Locate every blood parasite and identify its species.
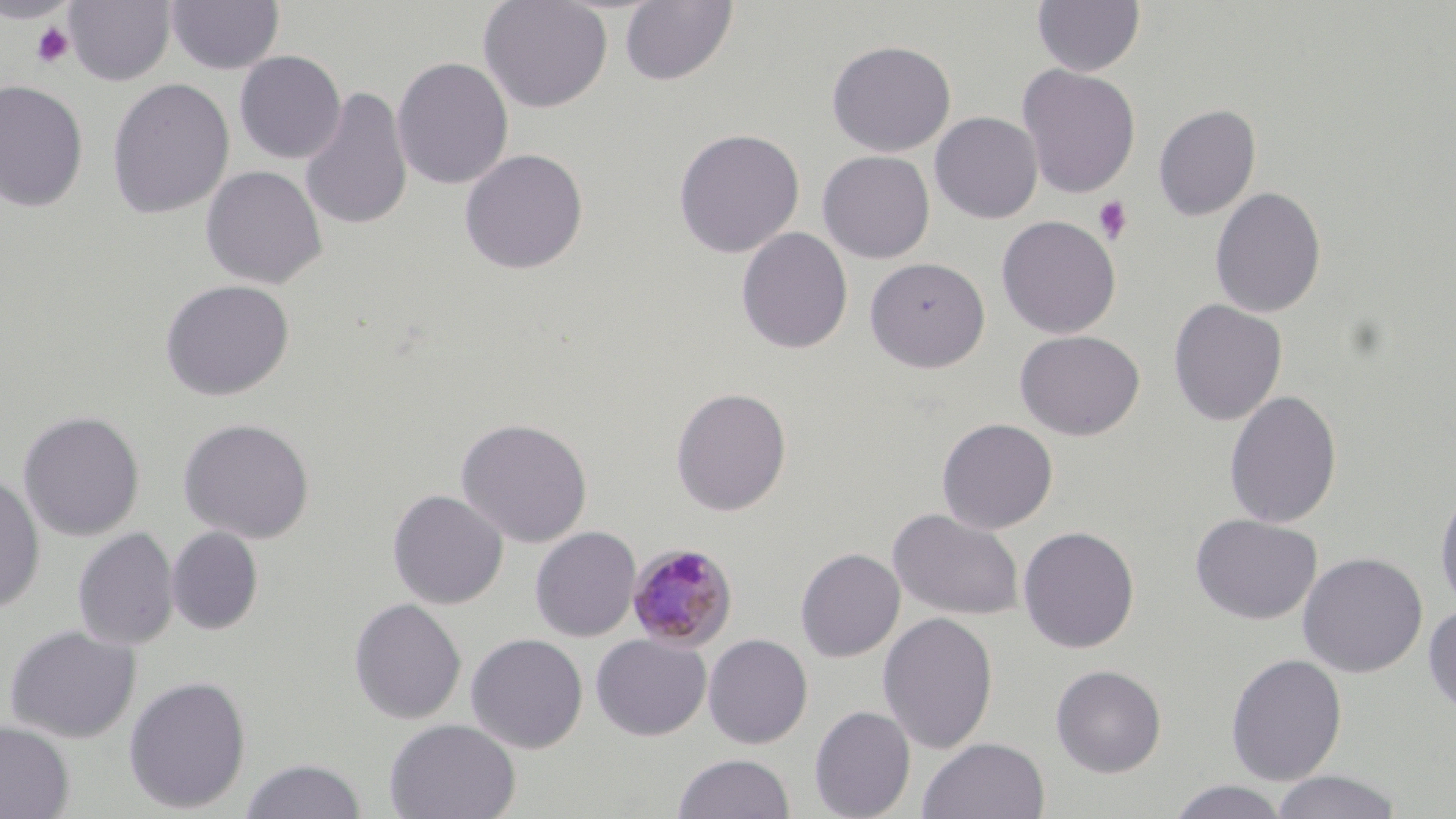
Approximate bounding boxes as named x1/y1/x2/y2 corners in pixels.
Plasmodium malariae-infected red blood cells: (x1=626, y1=542, x2=738, y2=652).
No Plasmodium falciparum, Plasmodium ovale, Plasmodium vivax, Babesia divergens, or Trypanosoma brucei observed.

Platelet locations: (x1=31, y1=21, x2=75, y2=68), (x1=1093, y1=196, x2=1132, y2=243). Uninfected red blood cell locations: (x1=0, y1=0, x2=80, y2=24), (x1=64, y1=0, x2=176, y2=86), (x1=166, y1=0, x2=284, y2=75), (x1=478, y1=0, x2=612, y2=114), (x1=1032, y1=0, x2=1146, y2=77), (x1=619, y1=1, x2=738, y2=86), (x1=18, y1=15, x2=82, y2=64), (x1=826, y1=39, x2=956, y2=157), (x1=234, y1=51, x2=346, y2=164), (x1=392, y1=57, x2=514, y2=190), (x1=1017, y1=64, x2=1141, y2=198), (x1=106, y1=78, x2=235, y2=220), (x1=0, y1=79, x2=89, y2=212), (x1=299, y1=85, x2=412, y2=231), (x1=1152, y1=103, x2=1261, y2=220), (x1=929, y1=112, x2=1043, y2=224), (x1=673, y1=128, x2=805, y2=258), (x1=459, y1=148, x2=588, y2=274), (x1=817, y1=150, x2=935, y2=263), (x1=201, y1=165, x2=326, y2=289), (x1=1210, y1=187, x2=1327, y2=318), (x1=996, y1=215, x2=1121, y2=338), (x1=736, y1=227, x2=853, y2=354), (x1=865, y1=257, x2=990, y2=372), (x1=159, y1=279, x2=295, y2=401), (x1=1168, y1=298, x2=1287, y2=425), (x1=1015, y1=330, x2=1144, y2=441), (x1=670, y1=387, x2=792, y2=516), (x1=1223, y1=390, x2=1342, y2=529), (x1=18, y1=410, x2=145, y2=541), (x1=178, y1=417, x2=315, y2=543), (x1=455, y1=417, x2=593, y2=548), (x1=937, y1=418, x2=1058, y2=534), (x1=0, y1=471, x2=44, y2=613), (x1=1434, y1=481, x2=1456, y2=615), (x1=387, y1=489, x2=508, y2=609), (x1=888, y1=508, x2=1024, y2=621), (x1=1190, y1=513, x2=1322, y2=625), (x1=531, y1=526, x2=641, y2=642), (x1=1017, y1=526, x2=1140, y2=654), (x1=73, y1=527, x2=179, y2=650), (x1=167, y1=527, x2=263, y2=635), (x1=795, y1=548, x2=905, y2=662), (x1=1298, y1=552, x2=1428, y2=678), (x1=348, y1=597, x2=466, y2=725), (x1=1422, y1=603, x2=1456, y2=717), (x1=878, y1=612, x2=998, y2=754), (x1=3, y1=624, x2=141, y2=743), (x1=466, y1=633, x2=588, y2=753), (x1=703, y1=633, x2=813, y2=749), (x1=591, y1=634, x2=711, y2=740), (x1=1225, y1=653, x2=1347, y2=785), (x1=1050, y1=664, x2=1167, y2=777), (x1=123, y1=675, x2=252, y2=814), (x1=809, y1=705, x2=915, y2=819), (x1=384, y1=718, x2=521, y2=819), (x1=0, y1=720, x2=75, y2=819), (x1=917, y1=736, x2=1050, y2=819), (x1=673, y1=753, x2=795, y2=818), (x1=241, y1=758, x2=367, y2=818), (x1=1270, y1=770, x2=1404, y2=819), (x1=1167, y1=780, x2=1292, y2=818). Slide-level diagnosis: Plasmodium malariae. Image is 1456×819 pixels. Thin blood film. May-Grünwald-Giemsa-stained preparation. 1000x magnification. Single field of view. Light microscopy.